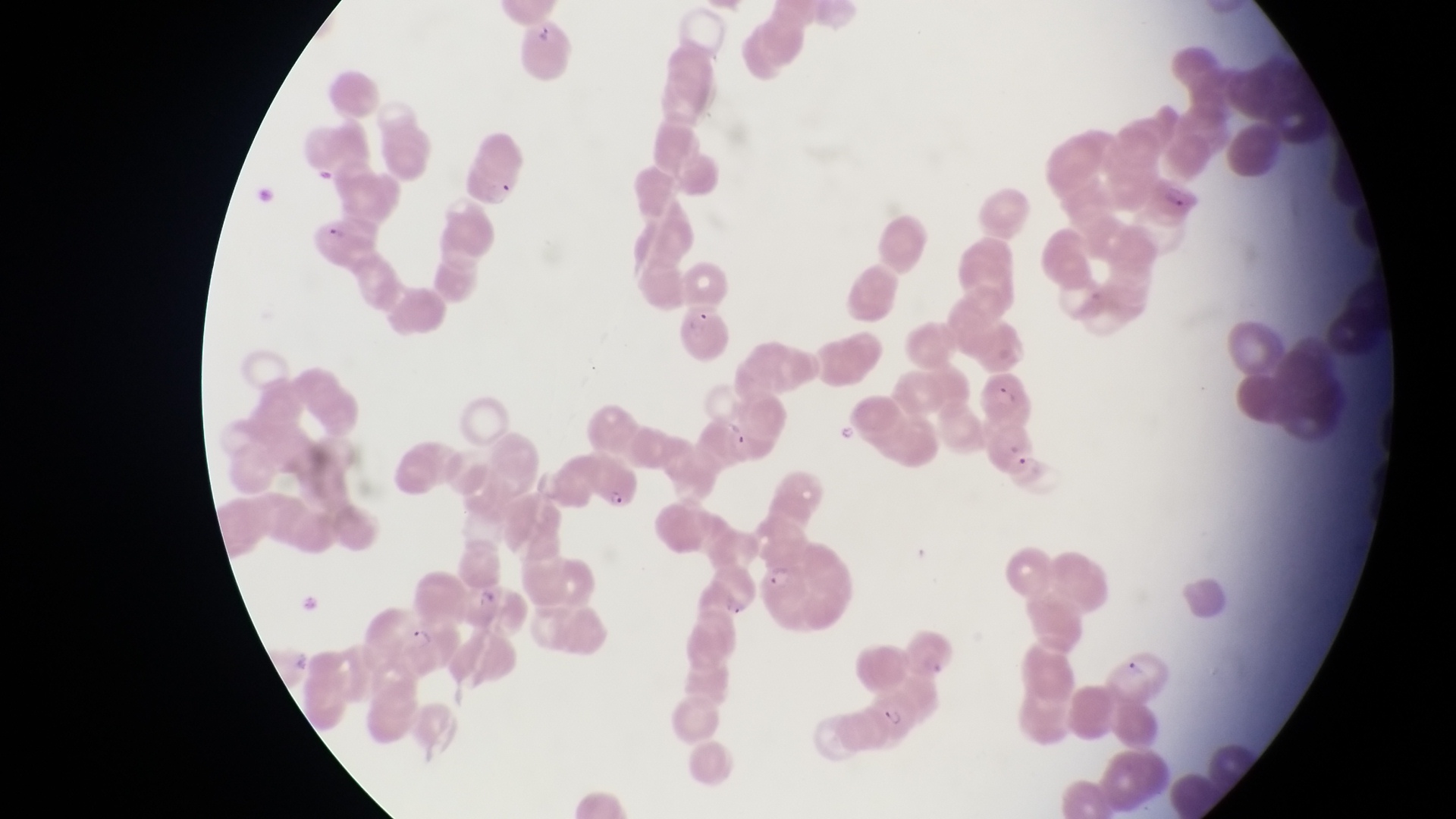
Approximate bounding boxes as [left, top, right, bottom] in pixels. Artifact (platelet-like body, stain precipitate, or debris) locations: [243, 184, 277, 207]. Parasitised red blood cell locations: [463, 152, 521, 208], [1150, 178, 1205, 224], [311, 212, 383, 262], [674, 298, 732, 359], [983, 376, 1036, 421], [576, 450, 643, 510], [758, 561, 811, 607], [462, 581, 529, 637], [396, 621, 462, 673], [867, 692, 917, 745]. Trophozoite locations: [1012, 452, 1045, 482]. Captured by a smartphone held over the eyepiece of an Olympus CX-23 microscope. One field of view. Image is 1456×819 pixels. Thin blood smear. Sample from Uganda. Magnification of 1000x.